State the preparation type.
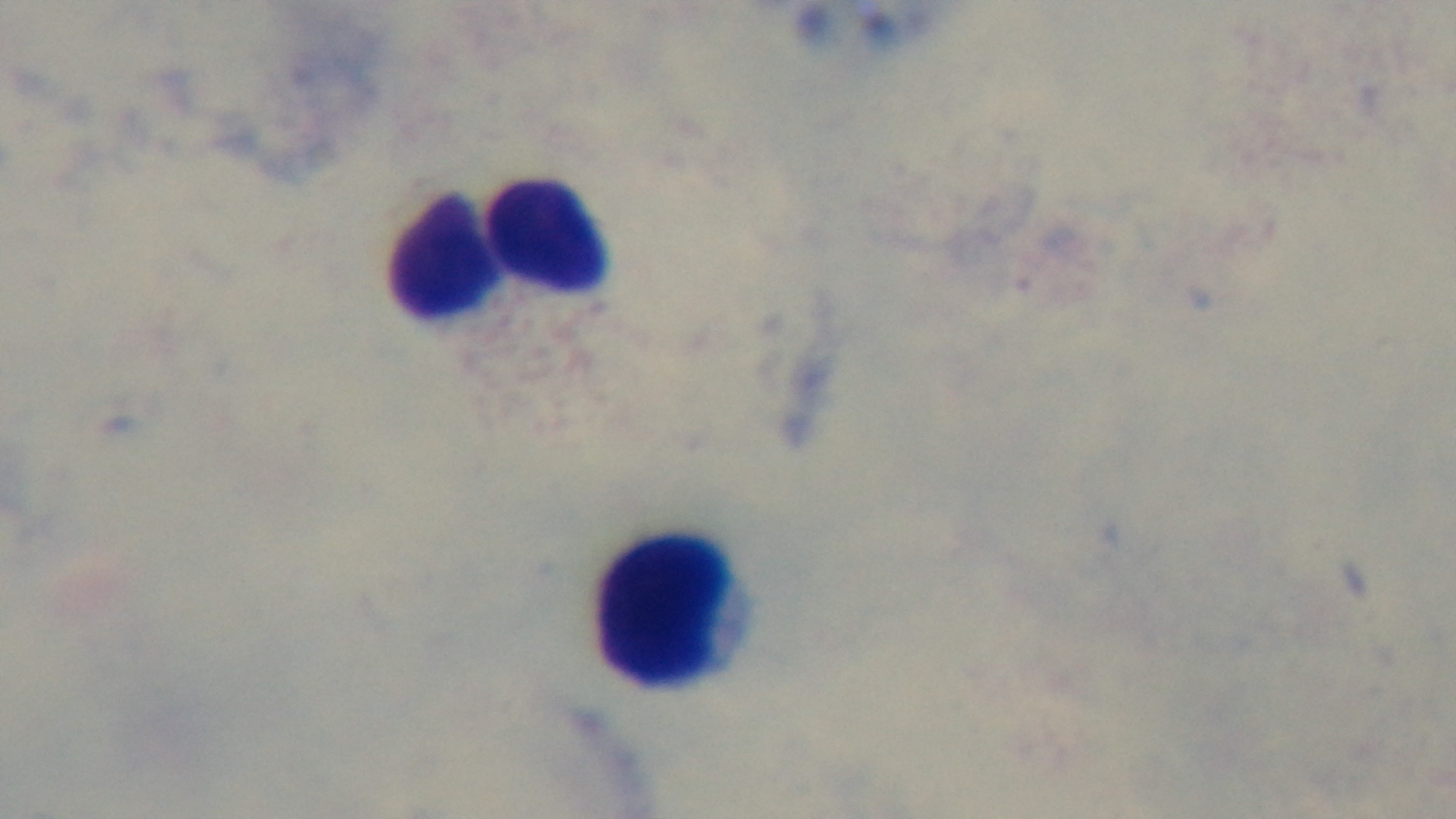

It is a thick blood film.

Photomicrograph. Captured with a mounted 4K digital camera. Malaria status: negative. Giemsa stain. Oil-immersion objective, 100x. Single field of view.